Describe the morphology of the erythrocytes.
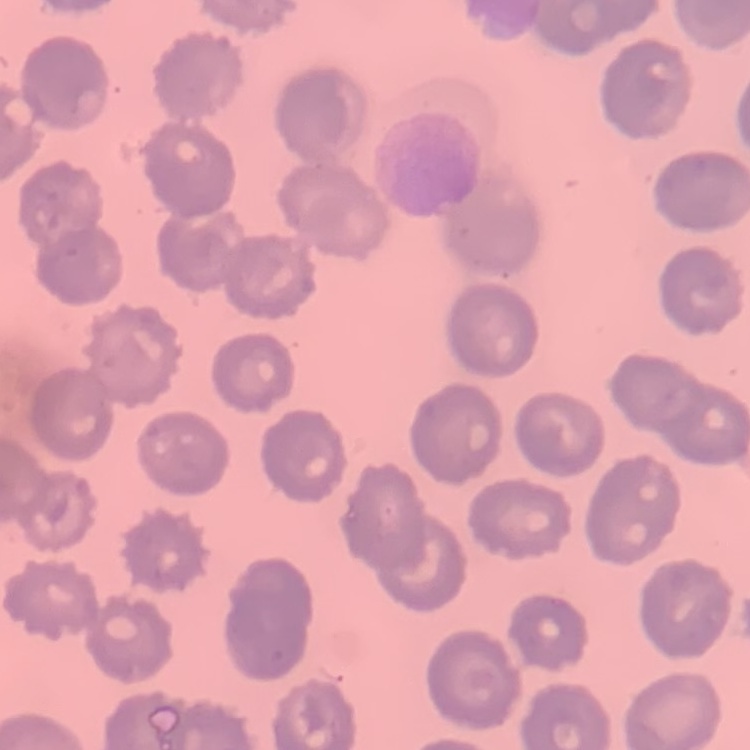
No rouleaux formation.

Summary:
  - Preparation: thin blood film
  - Stain: Field's or Giemsa
  - Image type: square crop of a larger photomicrograph